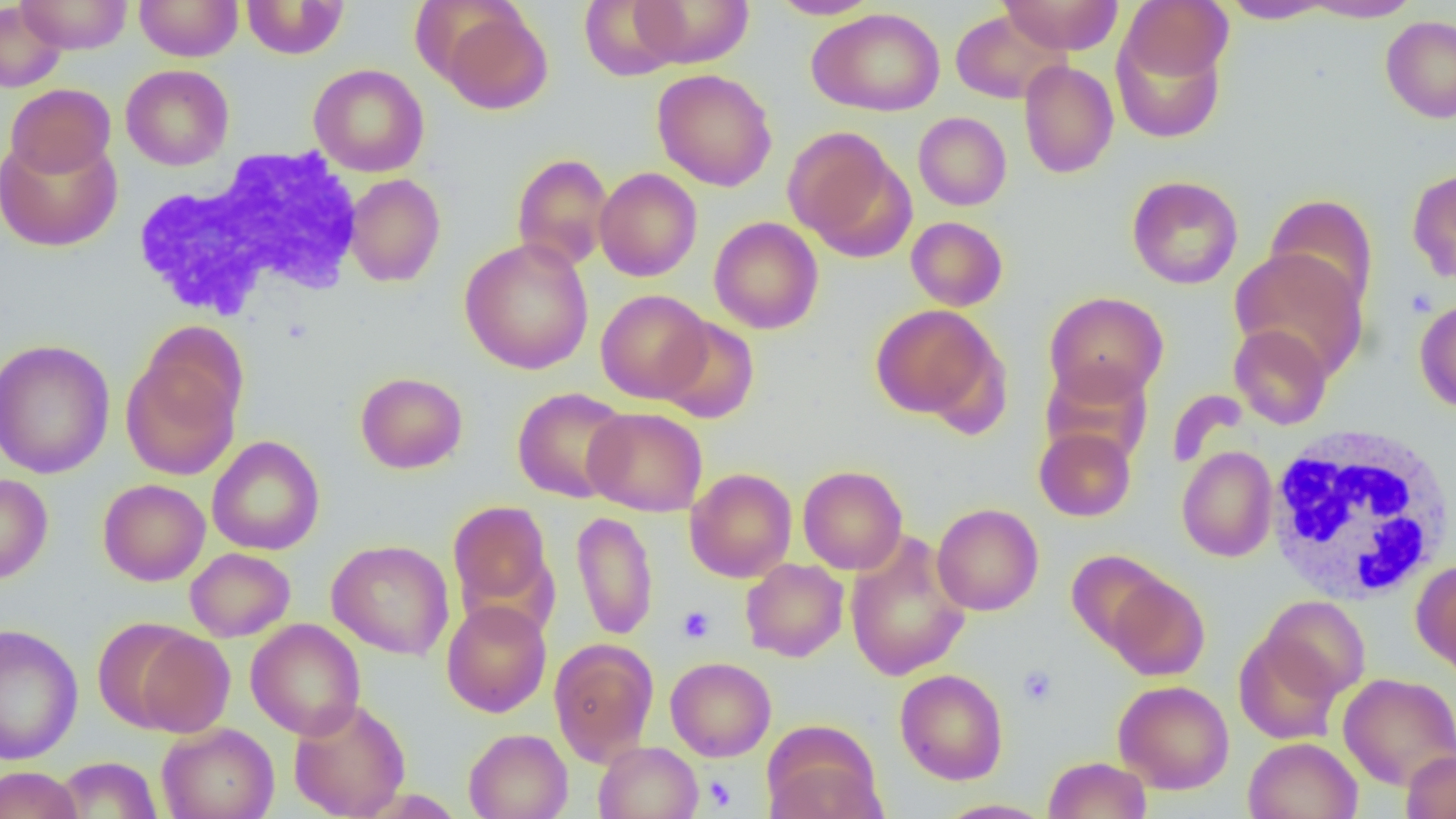
slide_level_diagnosis: negative for blood parasites
uninfected_red_blood_cell_locations: 'approximate bounding boxes as (x1,y1)-(x2,y2) corner pairs in pixels: (17,0)-(133,54), (134,0)-(243,61), (579,0)-(686,81), (628,0)-(755,68), (768,0)-(881,19), (999,0)-(1124,55), (1121,0)-(1233,84), (240,1)-(349,59), (1220,1)-(1335,23), (1299,1)-(1423,22), (0,2)-(67,93), (432,3)-(553,115), (807,8)-(946,116), (950,9)-(1069,104), (1380,16)-(1456,124), (1111,25)-(1227,144), (1019,60)-(1119,179), (121,64)-(234,170), (308,64)-(429,177), (651,68)-(777,191), (5,83)-(116,179), (913,111)-(1011,210), (783,127)-(913,259), (0,133)-(122,252), (512,153)-(613,272), (594,167)-(702,281), (1406,167)-(1456,284), (344,174)-(445,287), (1127,175)-(1243,289), (1264,194)-(1379,313), (709,216)-(823,334), (906,216)-(1008,311), (460,238)-(594,375), (1230,249)-(1368,380), (596,289)-(712,403), (1044,291)-(1169,403), (1414,297)-(1456,413), (870,304)-(1002,423), (656,317)-(760,423), (1229,324)-(1332,430), (0,338)-(115,479), (120,341)-(244,481), (1041,361)-(1153,465), (355,371)-(468,473), (512,387)-(632,503), (583,406)-(707,516), (1034,426)-(1137,521), (207,436)-(325,555), (1176,446)-(1278,562), (798,465)-(908,574), (685,467)-(797,582), (0,473)-(53,584), (98,478)-(211,586), (446,499)-(556,627), (931,503)-(1044,615), (572,511)-(659,641), (845,532)-(970,681), (327,539)-(454,660), (185,547)-(296,642), (1066,550)-(1172,652), (741,558)-(849,662), (1413,560)-(1456,677), (1104,572)-(1209,681), (1260,595)-(1370,701), (441,600)-(552,717), (246,619)-(366,740), (0,623)-(84,765), (124,626)-(236,737), (1234,631)-(1344,744), (549,638)-(659,765), (665,656)-(776,761), (894,668)-(1008,785), (1337,673)-(1456,790), (1113,680)-(1234,794), (288,698)-(411,819), (157,723)-(279,819), (763,724)-(887,819), (463,728)-(573,819), (1243,737)-(1362,819), (593,741)-(703,819), (1401,751)-(1456,818), (53,756)-(163,818), (1043,756)-(1152,818), (1,765)-(83,819), (935,799)-(1053,818)'
magnification: 1000x
preparation: thin blood film
field_of_view: one of a larger specimen
modality: optical microscopy
white_blood_cell_locations: 'approximate bounding boxes as (x1,y1)-(x2,y2) corner pairs in pixels: (133,146)-(366,325), (1263,423)-(1456,606)'
platelet_locations: 'approximate bounding boxes as (x1,y1)-(x2,y2) corner pairs in pixels: (1405,288)-(1438,319), (677,605)-(715,644), (1018,665)-(1057,706), (702,775)-(737,811)'
image_size: 1456×819 pixels